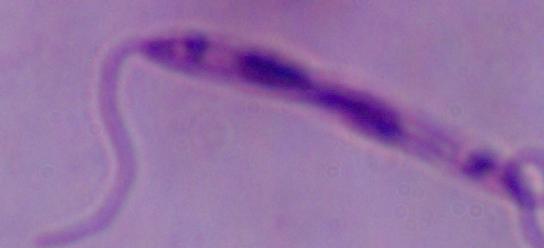
{
  "magnification": "1000x",
  "modality": "micrograph",
  "identification": "Leishmania"
}